Point out each malaria parasite and each leukocyte.
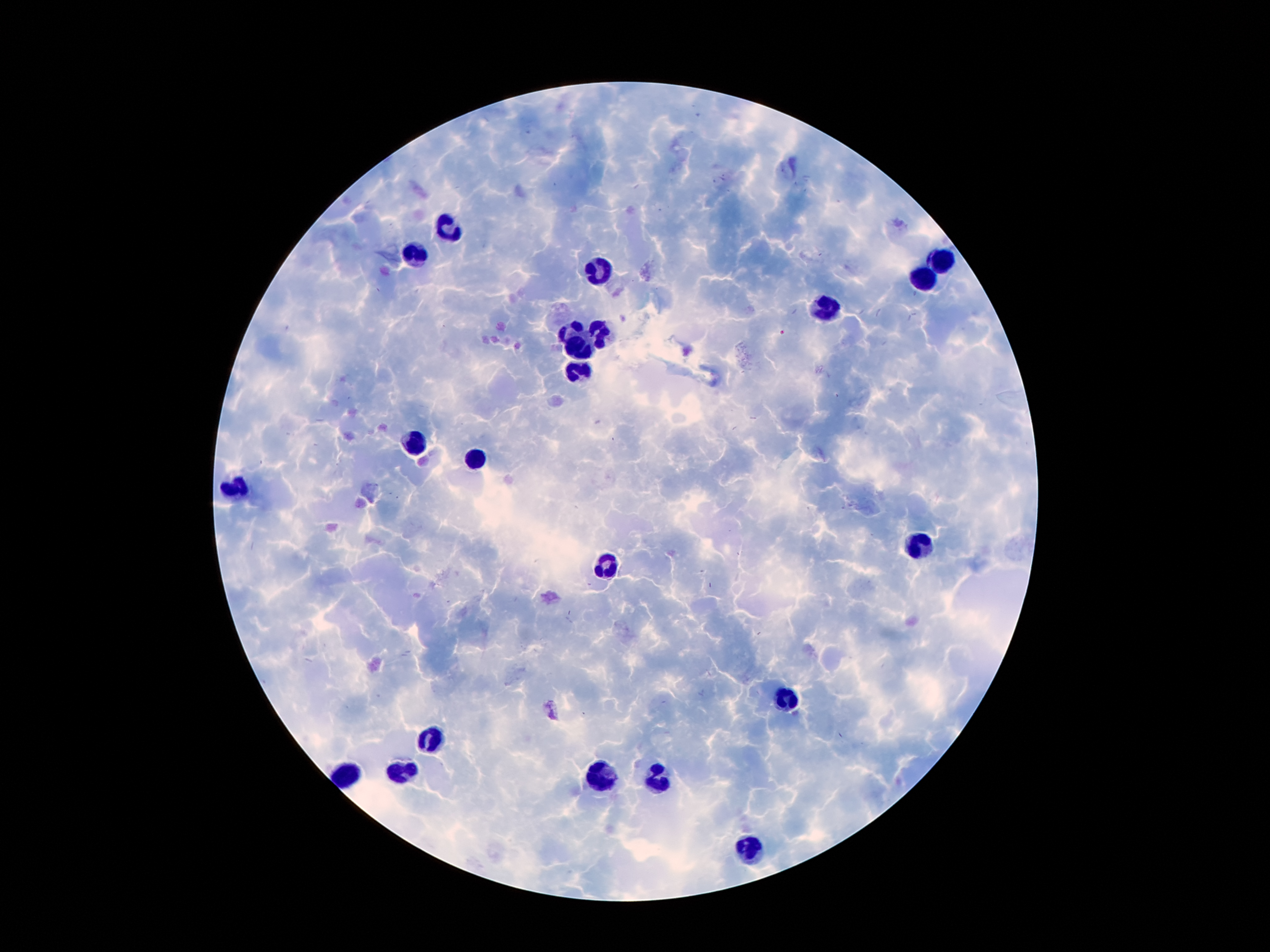

No malaria parasites detected.
Approximate object centers, in pixels from the top-left corner.
Leukocytes: (x=446, y=231), (x=412, y=253), (x=942, y=263), (x=601, y=272), (x=923, y=278), (x=828, y=309), (x=570, y=327), (x=604, y=332), (x=584, y=347), (x=579, y=372), (x=412, y=443), (x=473, y=460), (x=233, y=492), (x=917, y=542), (x=606, y=566), (x=787, y=700), (x=431, y=739), (x=404, y=771), (x=602, y=777), (x=659, y=777), (x=750, y=848).

field_of_view: single
capture: smartphone camera through the microscope eyepiece
image_size: 1270×952 pixels
preparation: thick blood film
magnification: 100x
stain: Giemsa
patient_malaria_status: positive for Plasmodium falciparum